Give the position of every malaria parasite.
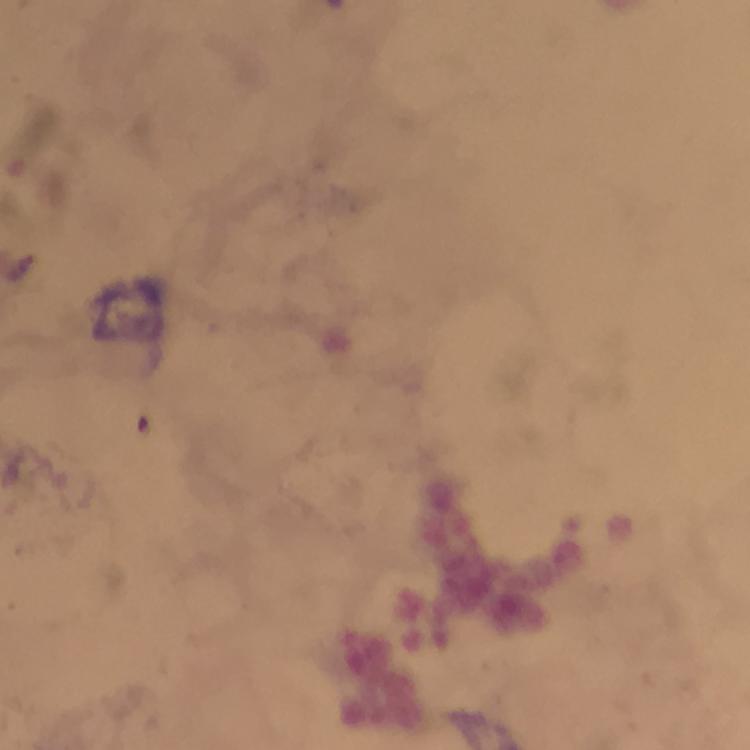

Approximate object centers, in pixels from the top-left corner.
Malaria parasites: (x=17, y=268).

magnification: 100x
capture: smartphone photograph through a microscope
image_size: 750×750 pixels
preparation: thick blood film
context: from a malaria diagnostic workup
immersion_oil: applied
cropped_from: one field of view
stain: Giemsa